Locate every P. falciparum parasite and give its life-cycle stage, and locate every leukocyte and any debris.
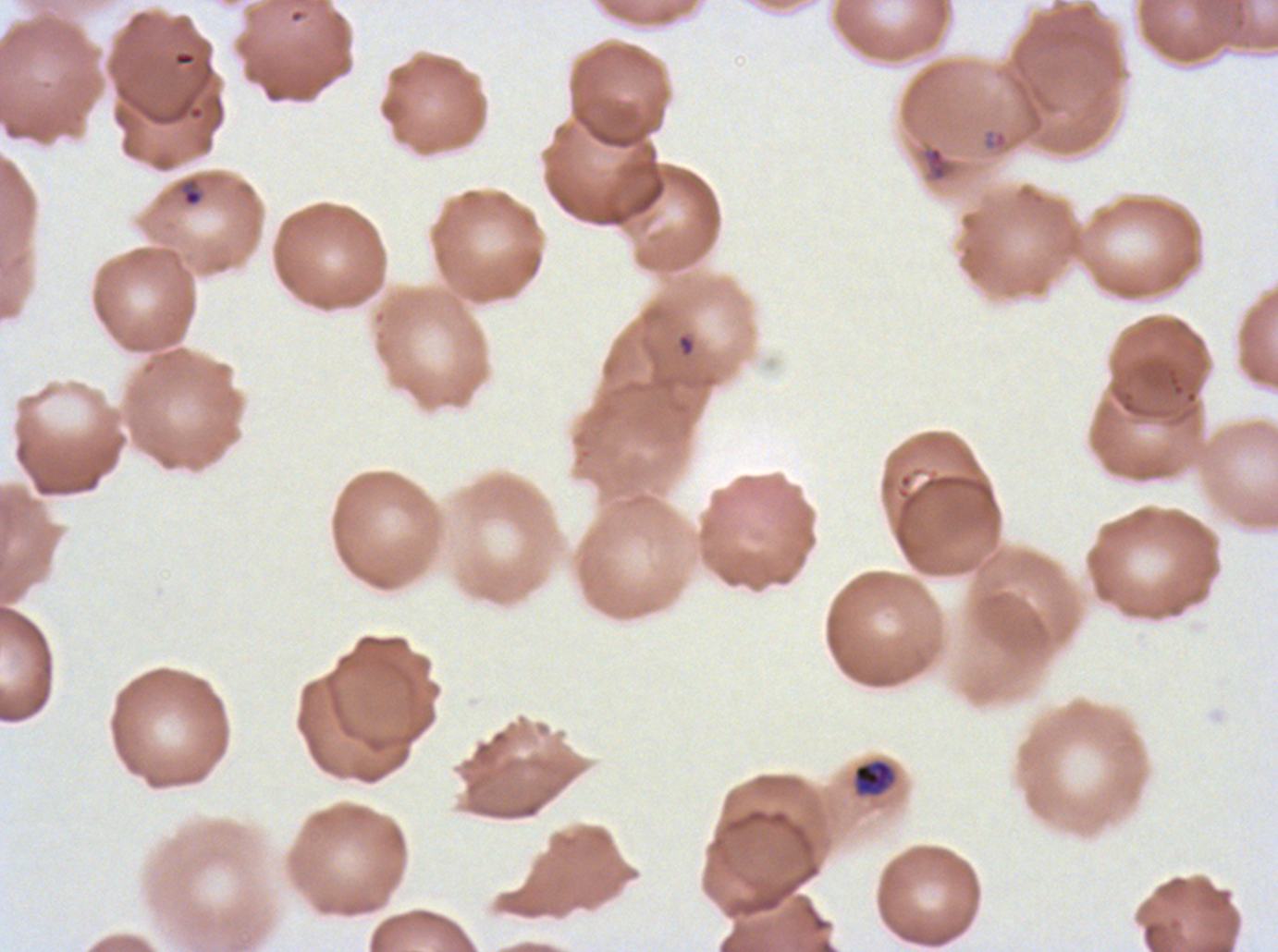

Approximate bounding boxes as (x1, y1, x2, y2) in pixels.
Rings: (178, 176, 204, 208), (679, 336, 694, 355).
Late-ring/early-trophozoite forms: (982, 128, 1009, 150), (922, 145, 948, 181), (854, 760, 893, 794).
Debris: (175, 52, 194, 66).
No mid trophozoites, late trophozoites, early schizonts, late schizonts, segmenters, gametocytes, or leukocytes observed.

Giemsa-stained preparation. A sub-image separated from a larger composite. Life-cycle stages observed: ring, late-ring/early-trophozoite. Thin blood film. P. falciparum cultured ex vivo for 24 to 48 hours, from a patient in The Gambia. Image is 1278×952 pixels.